State the blood parasite species.
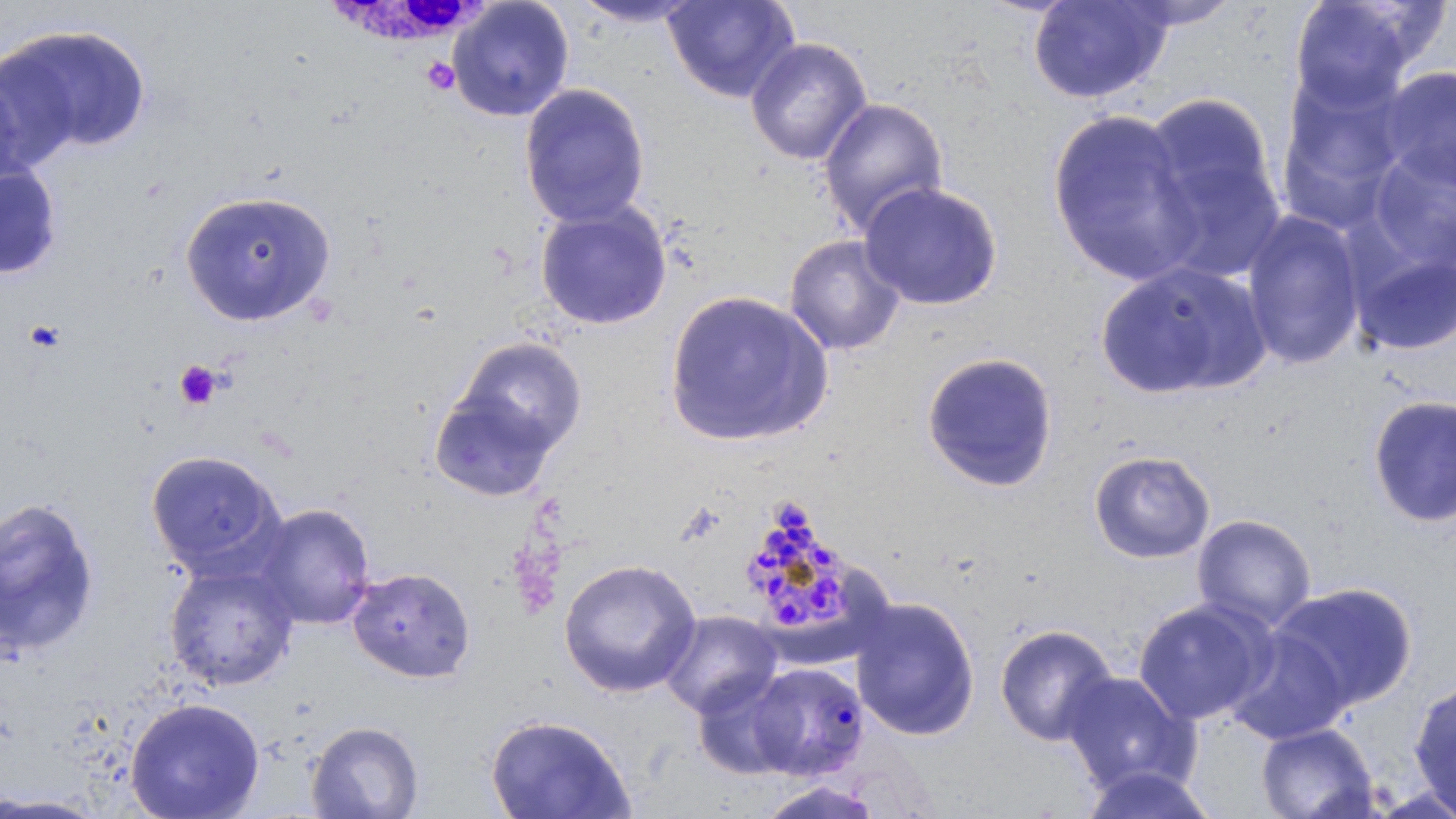
Plasmodium malariae.

Approximate bounding boxes as named x1/y1/x2/y2 corners in pixels. White blood cell locations: (x1=324, y1=0, x2=492, y2=54). Plasmodium malariae-infected red blood cell locations: (x1=739, y1=496, x2=859, y2=640), (x1=745, y1=661, x2=869, y2=780). Uninfected red blood cell locations: (x1=447, y1=0, x2=574, y2=122), (x1=568, y1=0, x2=706, y2=28), (x1=662, y1=0, x2=801, y2=103), (x1=1287, y1=0, x2=1427, y2=114), (x1=1027, y1=1, x2=1174, y2=104), (x1=1111, y1=1, x2=1245, y2=31), (x1=1, y1=23, x2=152, y2=158), (x1=745, y1=37, x2=873, y2=166), (x1=1374, y1=66, x2=1456, y2=191), (x1=0, y1=68, x2=40, y2=198), (x1=1275, y1=71, x2=1410, y2=226), (x1=519, y1=83, x2=650, y2=229), (x1=1139, y1=93, x2=1286, y2=282), (x1=818, y1=97, x2=948, y2=238), (x1=1046, y1=106, x2=1204, y2=288), (x1=1364, y1=143, x2=1456, y2=276), (x1=0, y1=161, x2=63, y2=280), (x1=859, y1=181, x2=1004, y2=311), (x1=179, y1=189, x2=337, y2=327), (x1=534, y1=200, x2=673, y2=331), (x1=1241, y1=210, x2=1367, y2=370), (x1=784, y1=234, x2=906, y2=357), (x1=1351, y1=247, x2=1456, y2=356), (x1=1095, y1=261, x2=1270, y2=399), (x1=663, y1=289, x2=834, y2=448), (x1=450, y1=336, x2=587, y2=464), (x1=920, y1=351, x2=1060, y2=493), (x1=427, y1=382, x2=564, y2=505), (x1=1367, y1=394, x2=1456, y2=528), (x1=1088, y1=449, x2=1216, y2=564), (x1=145, y1=450, x2=285, y2=579), (x1=0, y1=496, x2=102, y2=659), (x1=252, y1=503, x2=377, y2=630), (x1=1192, y1=514, x2=1316, y2=632), (x1=559, y1=558, x2=702, y2=698), (x1=163, y1=561, x2=300, y2=691), (x1=347, y1=566, x2=475, y2=683), (x1=1270, y1=582, x2=1420, y2=712), (x1=849, y1=595, x2=981, y2=741), (x1=1132, y1=597, x2=1276, y2=726), (x1=660, y1=610, x2=782, y2=718), (x1=993, y1=623, x2=1119, y2=747), (x1=1221, y1=625, x2=1352, y2=746), (x1=690, y1=670, x2=804, y2=779), (x1=1060, y1=670, x2=1196, y2=794), (x1=1409, y1=681, x2=1456, y2=816), (x1=124, y1=697, x2=266, y2=819), (x1=485, y1=714, x2=636, y2=819), (x1=306, y1=720, x2=425, y2=818), (x1=1255, y1=723, x2=1380, y2=819), (x1=1075, y1=763, x2=1220, y2=819), (x1=752, y1=780, x2=886, y2=819), (x1=0, y1=794, x2=110, y2=818). Platelet locations: (x1=421, y1=57, x2=461, y2=95), (x1=23, y1=318, x2=66, y2=354), (x1=175, y1=361, x2=222, y2=410). Single field of view. Image is 1456×819 pixels. Captured at 1000x magnification. May-Grünwald-Giemsa-stained preparation. Thin blood smear. Light microscopy.